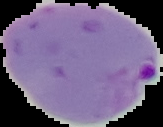
The area outside the segmented cell region is set to black. Malaria status: parasitized. Image is 163×127 pixels. From a thin blood film.